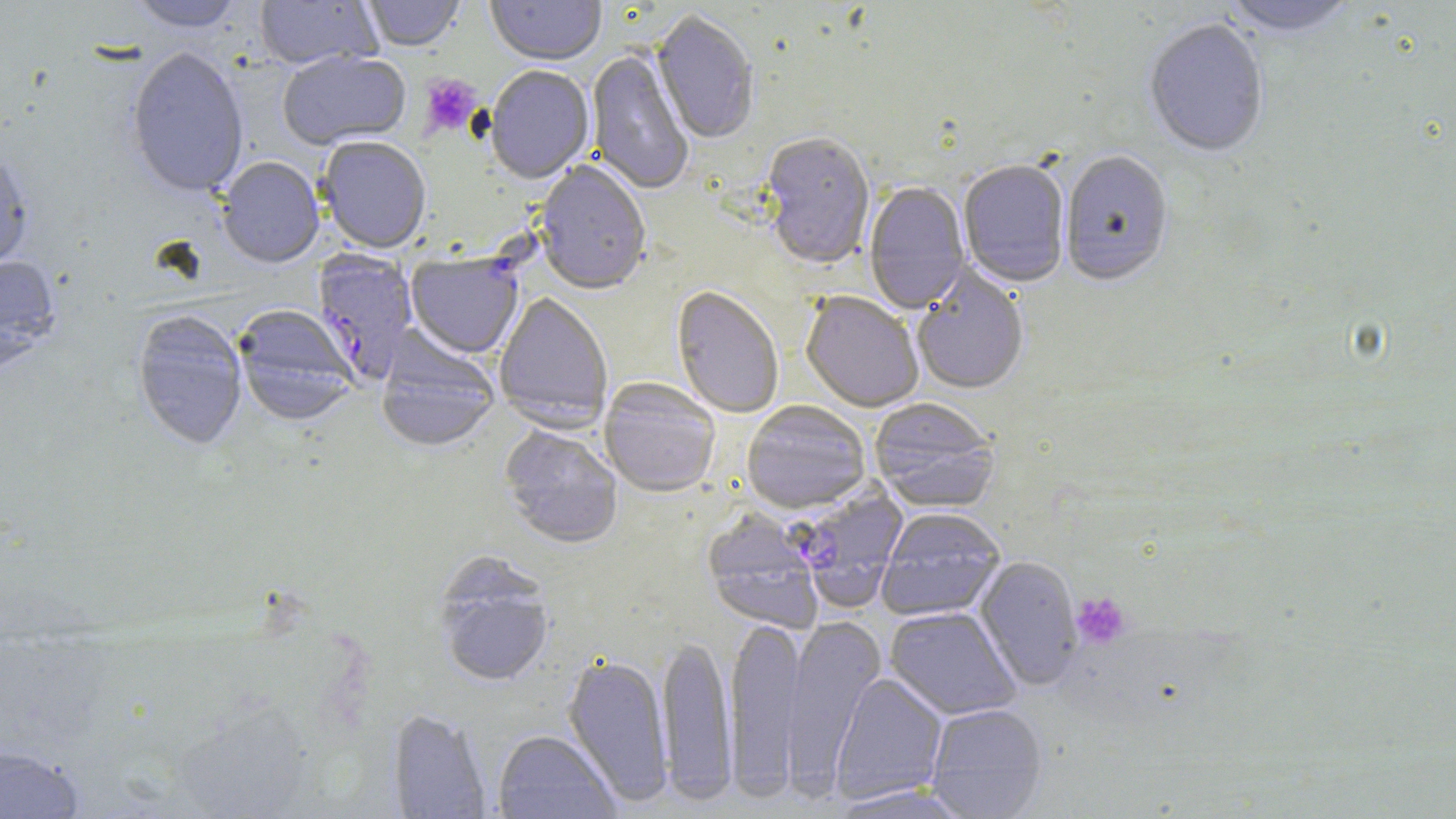
slide-level diagnosis = Plasmodium falciparum
magnification = 1000x
uninfected red blood cell locations = approximate bounding boxes as named x1/y1/x2/y2 corners in pixels: (x1=255, y1=0, x2=382, y2=72), (x1=358, y1=0, x2=465, y2=53), (x1=486, y1=0, x2=606, y2=68), (x1=1221, y1=0, x2=1359, y2=41), (x1=127, y1=1, x2=246, y2=32), (x1=651, y1=13, x2=759, y2=146), (x1=1143, y1=20, x2=1269, y2=160), (x1=126, y1=46, x2=249, y2=198), (x1=586, y1=49, x2=694, y2=197), (x1=278, y1=51, x2=411, y2=151), (x1=485, y1=67, x2=594, y2=186), (x1=759, y1=135, x2=875, y2=272), (x1=317, y1=139, x2=431, y2=254), (x1=0, y1=148, x2=34, y2=273), (x1=1060, y1=153, x2=1173, y2=289), (x1=217, y1=158, x2=324, y2=269), (x1=535, y1=162, x2=651, y2=296), (x1=957, y1=162, x2=1070, y2=290), (x1=864, y1=182, x2=971, y2=315), (x1=0, y1=254, x2=61, y2=372), (x1=911, y1=265, x2=1030, y2=398), (x1=671, y1=287, x2=784, y2=419), (x1=494, y1=293, x2=613, y2=432), (x1=801, y1=294, x2=923, y2=414), (x1=233, y1=306, x2=359, y2=425), (x1=132, y1=310, x2=248, y2=451), (x1=376, y1=333, x2=500, y2=454), (x1=599, y1=379, x2=721, y2=498), (x1=868, y1=399, x2=1000, y2=513), (x1=741, y1=401, x2=871, y2=514), (x1=499, y1=425, x2=623, y2=550), (x1=877, y1=509, x2=1006, y2=622), (x1=702, y1=511, x2=824, y2=635), (x1=974, y1=556, x2=1082, y2=692), (x1=435, y1=566, x2=554, y2=688), (x1=885, y1=607, x2=1021, y2=720), (x1=782, y1=614, x2=886, y2=797), (x1=725, y1=616, x2=806, y2=799), (x1=657, y1=634, x2=736, y2=804), (x1=562, y1=654, x2=674, y2=807), (x1=830, y1=673, x2=948, y2=806), (x1=926, y1=704, x2=1047, y2=818), (x1=388, y1=709, x2=492, y2=818), (x1=492, y1=731, x2=621, y2=818), (x1=0, y1=744, x2=85, y2=819), (x1=826, y1=784, x2=975, y2=818)
stain = May-Grünwald-Giemsa
image size = 1456×819 pixels
Plasmodium falciparum-infected red blood cell locations = approximate bounding boxes as named x1/y1/x2/y2 corners in pixels: (x1=312, y1=251, x2=419, y2=386), (x1=406, y1=255, x2=523, y2=360), (x1=792, y1=484, x2=908, y2=613)
platelet locations = approximate bounding boxes as named x1/y1/x2/y2 corners in pixels: (x1=419, y1=74, x2=482, y2=137), (x1=1071, y1=592, x2=1131, y2=649)
preparation = thin blood film
modality = optical microscopy
field of view = single